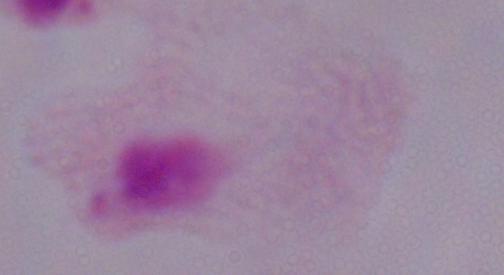

identification = trichomonad
modality = micrograph
magnification = 1000x